Assess this cell for malaria.
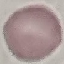

Uninfected.

Automatically extracted cell patch, resized to 64 × 64 pixels. Thin blood film. Giemsa stain. Acquired by smartphone through the microscope eyepiece.